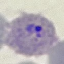
Malaria status: parasitized. Automatically extracted cell patch, resized to 64 × 64 pixels. Photographed with a smartphone camera at the microscope eyepiece. Giemsa stain. Thin blood smear.